Name the parasite shown.
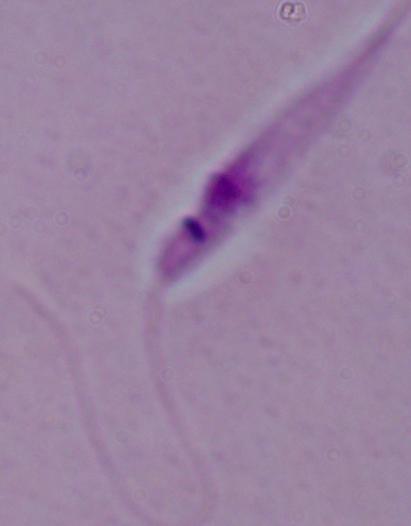

Leishmania.

magnification = 1000x
modality = photomicrograph